Describe the morphology of the erythrocytes.
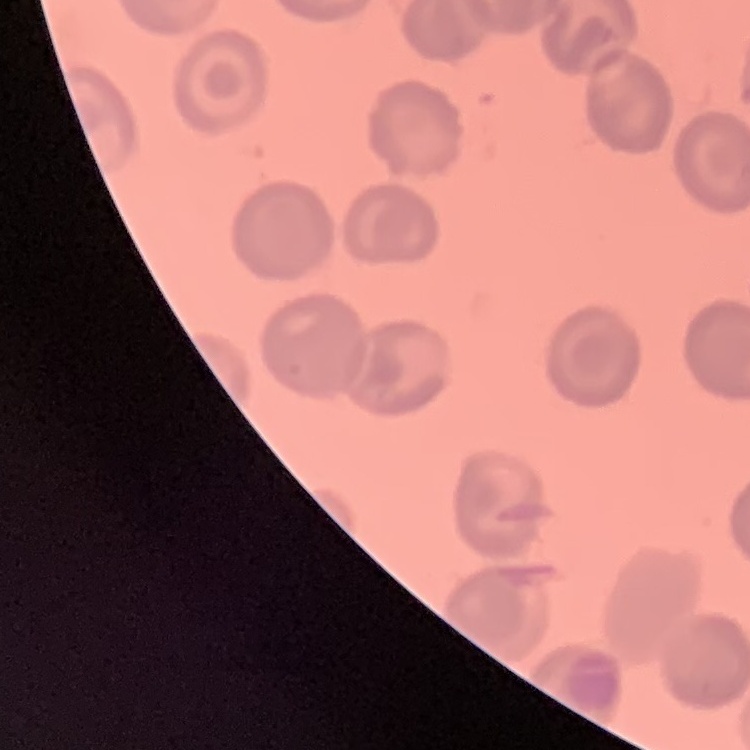

No rouleaux formation.

preparation: thin peripheral smear
stain: Field's or Giemsa
image_type: square crop of a larger photomicrograph